Point out each malaria parasite and each leukocyte.
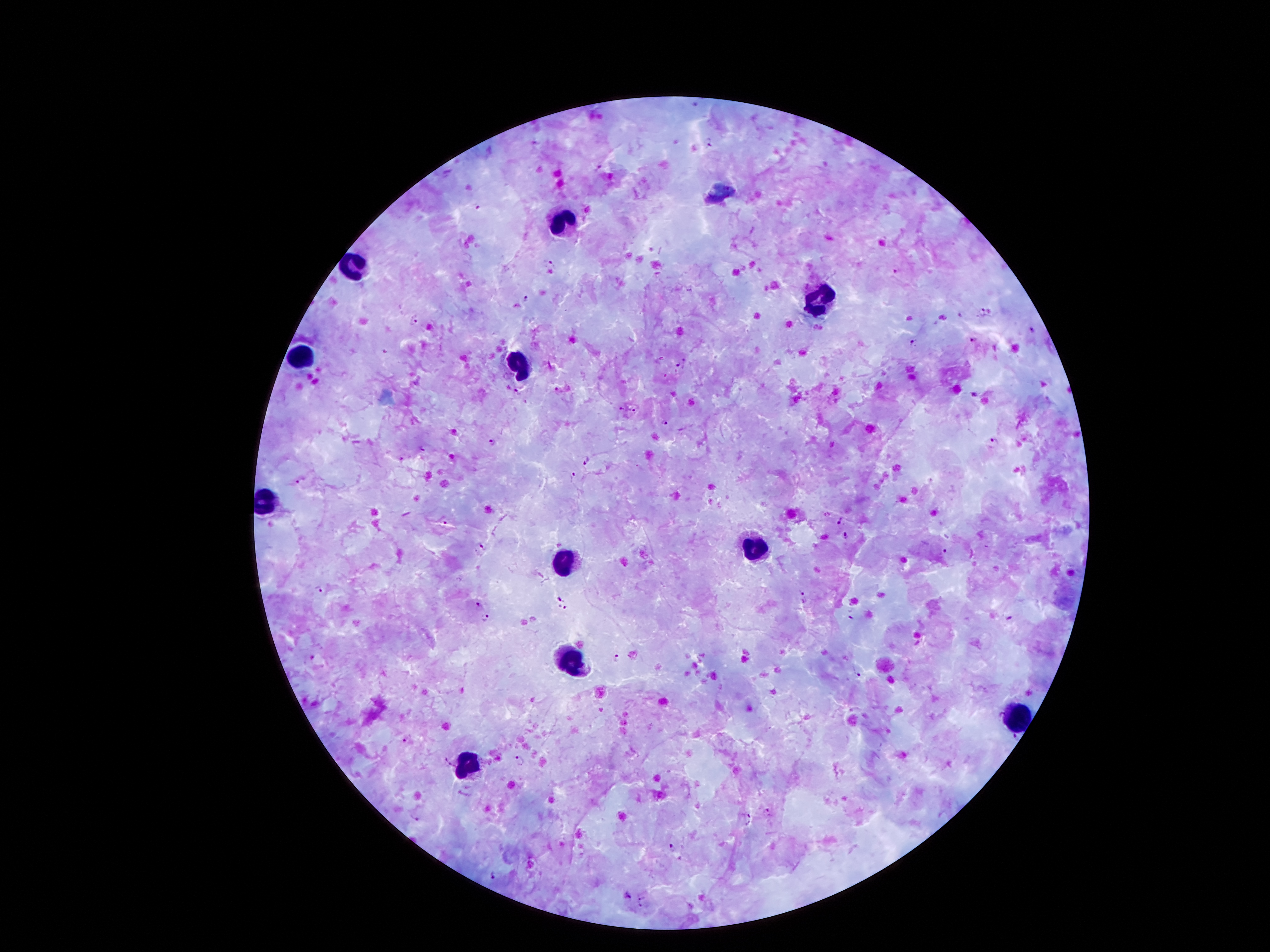

Approximate object centers, in pixels from the top-left corner.
Malaria parasites: (x=694, y=104), (x=537, y=140), (x=708, y=142), (x=598, y=167), (x=478, y=206), (x=551, y=264), (x=898, y=274), (x=526, y=297), (x=983, y=311), (x=414, y=320), (x=1033, y=332), (x=972, y=340), (x=913, y=342), (x=679, y=363), (x=517, y=390), (x=557, y=391), (x=974, y=395), (x=621, y=408), (x=634, y=410), (x=666, y=421), (x=992, y=440), (x=493, y=442), (x=588, y=459), (x=574, y=475), (x=300, y=482), (x=839, y=520), (x=445, y=522), (x=845, y=536), (x=484, y=547), (x=944, y=552), (x=319, y=587), (x=803, y=591), (x=559, y=598), (x=804, y=602), (x=478, y=605), (x=564, y=607), (x=486, y=618), (x=850, y=618), (x=1009, y=619), (x=616, y=658), (x=859, y=675), (x=407, y=740), (x=519, y=760), (x=449, y=761), (x=768, y=812), (x=417, y=818), (x=747, y=819), (x=671, y=846), (x=492, y=876), (x=626, y=896), (x=642, y=902).
Leukocytes: (x=564, y=221), (x=349, y=266), (x=816, y=305), (x=302, y=359), (x=517, y=361), (x=267, y=504), (x=756, y=547), (x=560, y=560), (x=574, y=660), (x=1019, y=717), (x=470, y=766).

Summary:
  - Magnification: 100x
  - Stain: Giemsa
  - Preparation: thick blood film
  - Image size: 1270×952 pixels
  - Patient malaria status: positive for Plasmodium falciparum
  - Capture: smartphone camera through the microscope eyepiece
  - Field of view: single